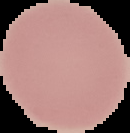
Summary:
  - Result: no malaria parasites seen
  - Image type: segmented cell region on a black background
  - Image size: 130×133 pixels
  - Preparation: thin blood film